State which parasite is depicted.
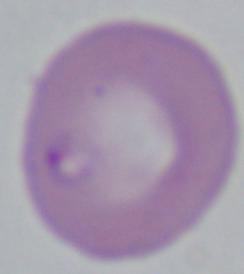
This is Babesia.

Captured at 1000x magnification. Micrograph.